Locate every malaria parasite and identify its life-cycle stage.
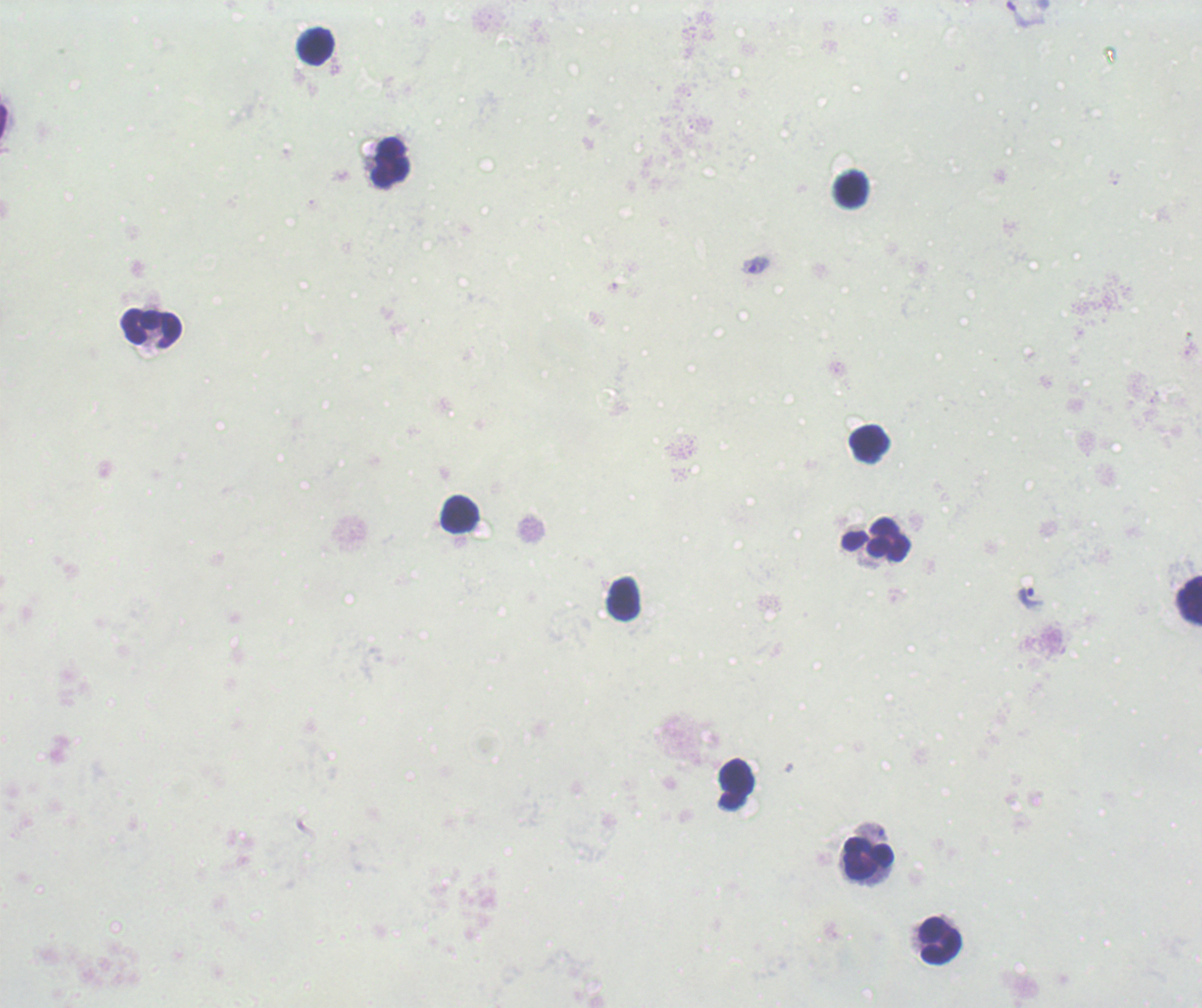
Approximate object centers, in pixels from the top-left corner.
Trophozoites: (x=754, y=265), (x=1030, y=597).
No schizont or gametocyte forms observed.

Approximate object centers, in pixels from the top-left corner.
Summary:
  - Leukocyte locations: (x=315, y=46), (x=391, y=162), (x=851, y=189), (x=151, y=328), (x=868, y=443), (x=459, y=515), (x=876, y=540), (x=623, y=599), (x=1189, y=600), (x=736, y=784), (x=868, y=858), (x=941, y=941)
  - Magnification: 100x
  - Image size: 1202×1008 pixels
  - Context: previously used in an actual diagnosis
  - Background quality: unsatisfactory
  - Field of view: single
  - Preparation: thick smear of blood
  - Stain: Romanowsky